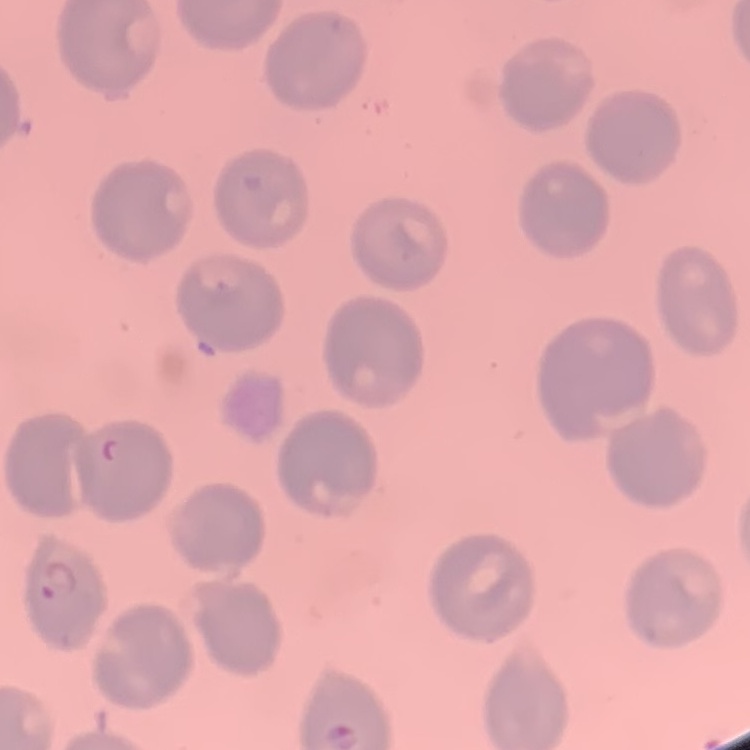

The red blood cells exhibit no rouleaux formation. Thin peripheral smear. Stained with either Field's or Giemsa. Square crop of a larger photomicrograph.